Report the malaria status of this cell.
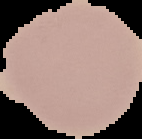
Uninfected.

Summary:
  - Preparation: thin blood film
  - Image size: 142×139 pixels
  - Image type: segmented cell region on a black background